Describe the morphology of the red blood cells.
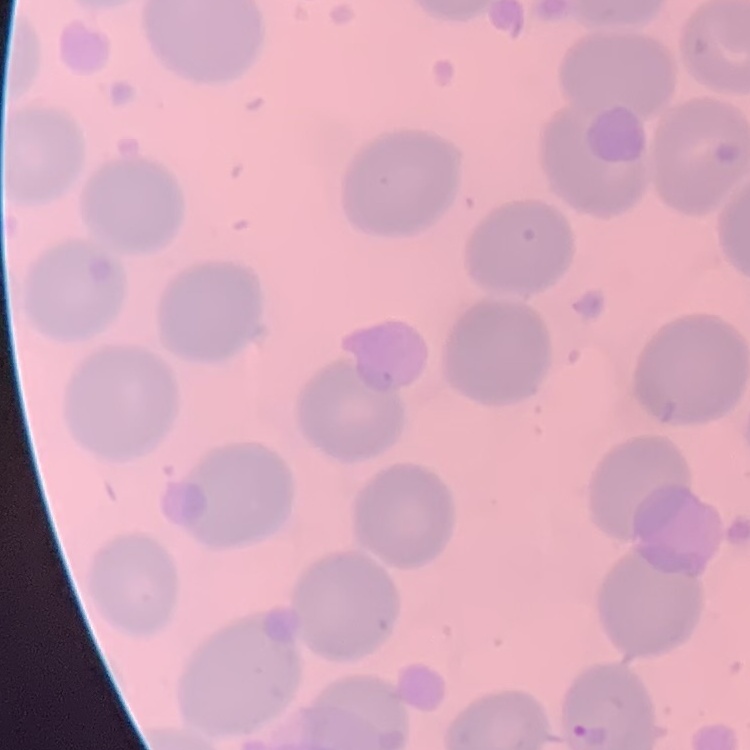

They show no rouleaux formation.

stain = Field's or Giemsa
preparation = thin peripheral smear
image type = square crop of a larger photomicrograph